Identify the parasite.
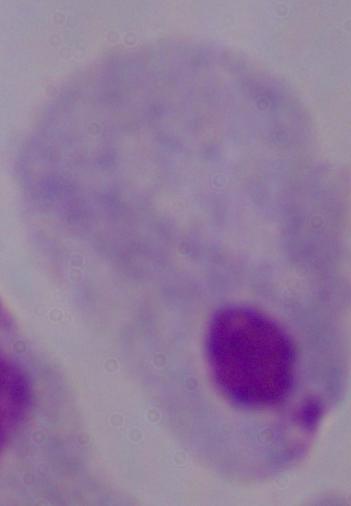

This is a trichomonad.

Summary:
  - Modality: photomicrograph
  - Magnification: 1000x